Locate and identify every blood parasite.
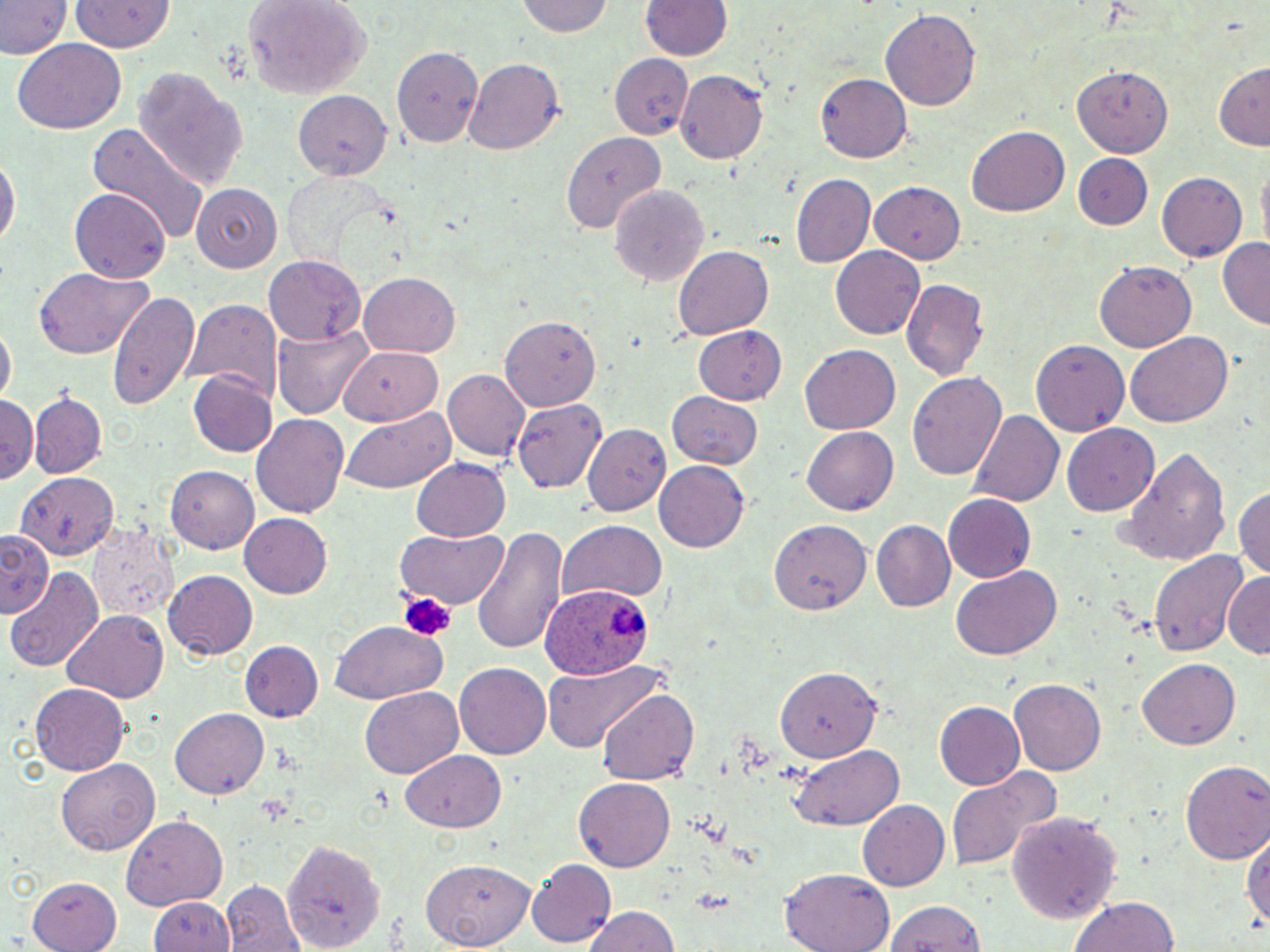

Approximate bounding boxes as named x1/y1/x2/y2 corners in pixels.
Plasmodium ovale-infected red blood cells: (x1=542, y1=585, x2=653, y2=682).
No Plasmodium falciparum, Plasmodium malariae, Plasmodium vivax, Babesia divergens, or Trypanosoma brucei observed.

Uninfected red blood cell locations: (x1=0, y1=0, x2=68, y2=60), (x1=243, y1=0, x2=371, y2=99), (x1=515, y1=0, x2=616, y2=39), (x1=70, y1=1, x2=174, y2=57), (x1=641, y1=1, x2=733, y2=63), (x1=881, y1=8, x2=978, y2=113), (x1=12, y1=40, x2=125, y2=135), (x1=391, y1=44, x2=485, y2=147), (x1=611, y1=50, x2=688, y2=138), (x1=464, y1=58, x2=565, y2=157), (x1=1214, y1=61, x2=1268, y2=150), (x1=1070, y1=64, x2=1168, y2=196), (x1=676, y1=69, x2=767, y2=163), (x1=134, y1=71, x2=249, y2=191), (x1=816, y1=73, x2=910, y2=163), (x1=292, y1=92, x2=391, y2=179), (x1=86, y1=124, x2=211, y2=251), (x1=964, y1=127, x2=1070, y2=218), (x1=561, y1=130, x2=663, y2=235), (x1=0, y1=151, x2=17, y2=257), (x1=1073, y1=155, x2=1153, y2=232), (x1=1255, y1=160, x2=1270, y2=253), (x1=1155, y1=171, x2=1248, y2=263), (x1=282, y1=173, x2=395, y2=269), (x1=790, y1=173, x2=875, y2=268), (x1=609, y1=183, x2=708, y2=285), (x1=868, y1=183, x2=964, y2=264), (x1=192, y1=184, x2=282, y2=271), (x1=71, y1=189, x2=170, y2=285), (x1=1217, y1=236, x2=1270, y2=328), (x1=674, y1=247, x2=774, y2=339), (x1=831, y1=248, x2=924, y2=338), (x1=266, y1=255, x2=364, y2=343), (x1=1093, y1=262, x2=1197, y2=352), (x1=33, y1=268, x2=156, y2=359), (x1=359, y1=272, x2=462, y2=357), (x1=901, y1=278, x2=989, y2=383), (x1=106, y1=288, x2=201, y2=409), (x1=183, y1=299, x2=278, y2=394), (x1=500, y1=317, x2=598, y2=408), (x1=271, y1=323, x2=372, y2=419), (x1=1, y1=325, x2=16, y2=402), (x1=693, y1=327, x2=785, y2=406), (x1=1125, y1=333, x2=1232, y2=428), (x1=1032, y1=340, x2=1128, y2=436), (x1=338, y1=345, x2=445, y2=426), (x1=799, y1=345, x2=900, y2=435), (x1=189, y1=370, x2=274, y2=458), (x1=441, y1=370, x2=529, y2=462), (x1=907, y1=371, x2=1008, y2=484), (x1=30, y1=391, x2=105, y2=479), (x1=666, y1=393, x2=764, y2=470), (x1=0, y1=396, x2=38, y2=484), (x1=514, y1=397, x2=609, y2=491), (x1=339, y1=407, x2=457, y2=492), (x1=968, y1=409, x2=1066, y2=507), (x1=253, y1=414, x2=350, y2=519), (x1=1062, y1=423, x2=1161, y2=516), (x1=582, y1=424, x2=670, y2=516), (x1=800, y1=426, x2=897, y2=515), (x1=1125, y1=446, x2=1231, y2=567), (x1=409, y1=457, x2=510, y2=542), (x1=653, y1=461, x2=752, y2=554), (x1=167, y1=466, x2=258, y2=554), (x1=17, y1=475, x2=117, y2=562), (x1=1236, y1=483, x2=1270, y2=584), (x1=943, y1=493, x2=1036, y2=583), (x1=240, y1=513, x2=333, y2=597), (x1=86, y1=517, x2=182, y2=625), (x1=559, y1=519, x2=667, y2=603), (x1=770, y1=520, x2=872, y2=615), (x1=869, y1=520, x2=955, y2=613), (x1=396, y1=526, x2=507, y2=611), (x1=0, y1=527, x2=55, y2=616), (x1=469, y1=527, x2=566, y2=655), (x1=1150, y1=548, x2=1248, y2=659), (x1=951, y1=567, x2=1061, y2=660), (x1=9, y1=569, x2=103, y2=672), (x1=164, y1=570, x2=258, y2=660), (x1=1223, y1=571, x2=1269, y2=658), (x1=61, y1=610, x2=169, y2=702), (x1=333, y1=620, x2=448, y2=705), (x1=240, y1=639, x2=323, y2=723), (x1=1139, y1=657, x2=1241, y2=749), (x1=542, y1=660, x2=664, y2=753), (x1=453, y1=663, x2=550, y2=759), (x1=775, y1=665, x2=891, y2=763), (x1=1009, y1=679, x2=1104, y2=775), (x1=30, y1=683, x2=131, y2=775), (x1=361, y1=687, x2=463, y2=777), (x1=598, y1=688, x2=697, y2=786), (x1=933, y1=701, x2=1024, y2=791), (x1=170, y1=708, x2=269, y2=800), (x1=788, y1=745, x2=907, y2=831), (x1=401, y1=750, x2=506, y2=833), (x1=1180, y1=760, x2=1270, y2=866), (x1=58, y1=761, x2=158, y2=855), (x1=946, y1=768, x2=1056, y2=870), (x1=573, y1=779, x2=676, y2=870), (x1=858, y1=798, x2=951, y2=892), (x1=1007, y1=809, x2=1122, y2=922), (x1=123, y1=815, x2=227, y2=908), (x1=1243, y1=824, x2=1270, y2=940), (x1=284, y1=839, x2=386, y2=952), (x1=422, y1=858, x2=536, y2=946), (x1=526, y1=859, x2=614, y2=944), (x1=779, y1=870, x2=895, y2=952), (x1=28, y1=871, x2=120, y2=950), (x1=222, y1=881, x2=304, y2=952), (x1=151, y1=894, x2=235, y2=951), (x1=1068, y1=896, x2=1179, y2=952), (x1=881, y1=898, x2=987, y2=952), (x1=584, y1=904, x2=680, y2=952). Platelet locations: (x1=396, y1=590, x2=457, y2=643). Slide-level diagnosis: Plasmodium ovale. Thin blood smear. Captured at 1000x magnification. Light microscopy. Single field of view. Image is 1270×952 pixels. May-Grünwald-Giemsa stain.